Name the parasite shown.
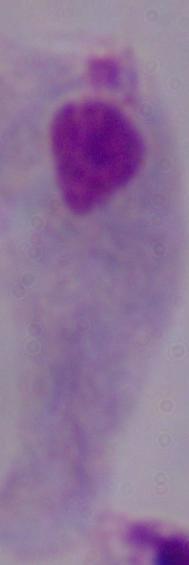
A trichomonad.

modality = photomicrograph
magnification = 1000x